Give the extent of all white blood cells.
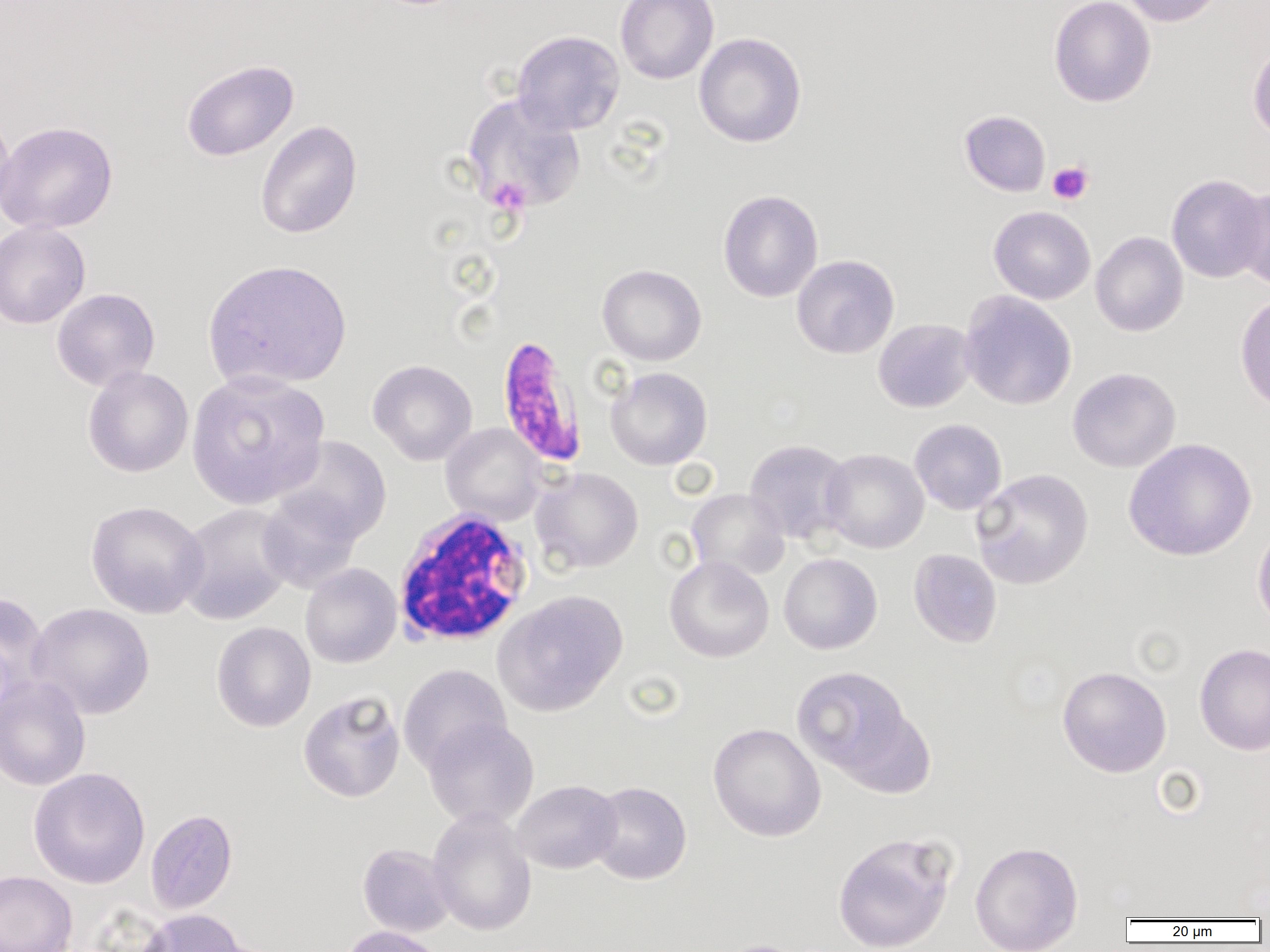
Approximate bounding boxes as [x1, y1, x2, y2] in pixels.
White blood cells: [393, 508, 534, 646].

Summary:
  - Uninfected red blood cell locations: [615, 0, 719, 84], [1049, 0, 1156, 107], [1118, 0, 1224, 27], [511, 30, 625, 136], [694, 32, 807, 148], [1247, 40, 1270, 144], [181, 59, 299, 162], [461, 93, 587, 213], [0, 105, 16, 222], [959, 110, 1051, 196], [0, 120, 118, 234], [255, 120, 362, 239], [1166, 173, 1268, 284], [1232, 184, 1270, 292], [718, 189, 823, 302], [988, 206, 1096, 304], [0, 220, 91, 330], [1090, 231, 1189, 337], [791, 254, 900, 359], [202, 258, 352, 392], [597, 264, 707, 366], [51, 288, 160, 391], [959, 291, 1077, 410], [1235, 292, 1270, 414], [873, 318, 976, 413], [368, 359, 477, 465], [82, 366, 194, 478], [605, 367, 712, 470], [1067, 368, 1181, 473], [185, 369, 330, 509], [909, 419, 1007, 515], [441, 423, 546, 525], [273, 435, 392, 544], [1123, 438, 1257, 561], [743, 439, 853, 545], [820, 448, 929, 553], [971, 467, 1094, 590], [531, 468, 643, 573], [686, 488, 789, 581], [256, 490, 364, 594], [85, 500, 209, 619], [176, 503, 296, 625], [1252, 523, 1270, 633], [908, 548, 1002, 648], [778, 553, 882, 654], [664, 555, 774, 663], [300, 563, 402, 669], [0, 590, 50, 707], [493, 590, 629, 716], [27, 602, 154, 720], [211, 621, 316, 732], [1194, 643, 1270, 756], [398, 664, 512, 774], [791, 665, 915, 782], [1057, 665, 1172, 778], [0, 676, 91, 791], [298, 690, 406, 803], [422, 718, 539, 829], [708, 723, 826, 842], [28, 767, 151, 889], [512, 780, 622, 874], [588, 781, 692, 885], [145, 808, 238, 914], [427, 809, 537, 936], [832, 832, 957, 952], [970, 840, 1083, 952], [357, 843, 455, 937], [0, 871, 77, 952], [136, 908, 248, 952], [340, 925, 445, 952], [714, 938, 815, 952]
  - Platelet locations: [1047, 161, 1094, 205], [487, 177, 530, 216]
  - Plasmodium falciparum-infected red blood cell locations: [495, 335, 589, 469]
  - Slide-level diagnosis: Plasmodium falciparum
  - Preparation: thin blood film
  - Magnification: 1000x
  - Image size: 1270×952 pixels
  - Field of view: one of a larger specimen
  - Modality: optical microscopy